Draw a bounding box around every Plasmodium parasite, every leukocyte, and every artifact (stain precipitate or debris).
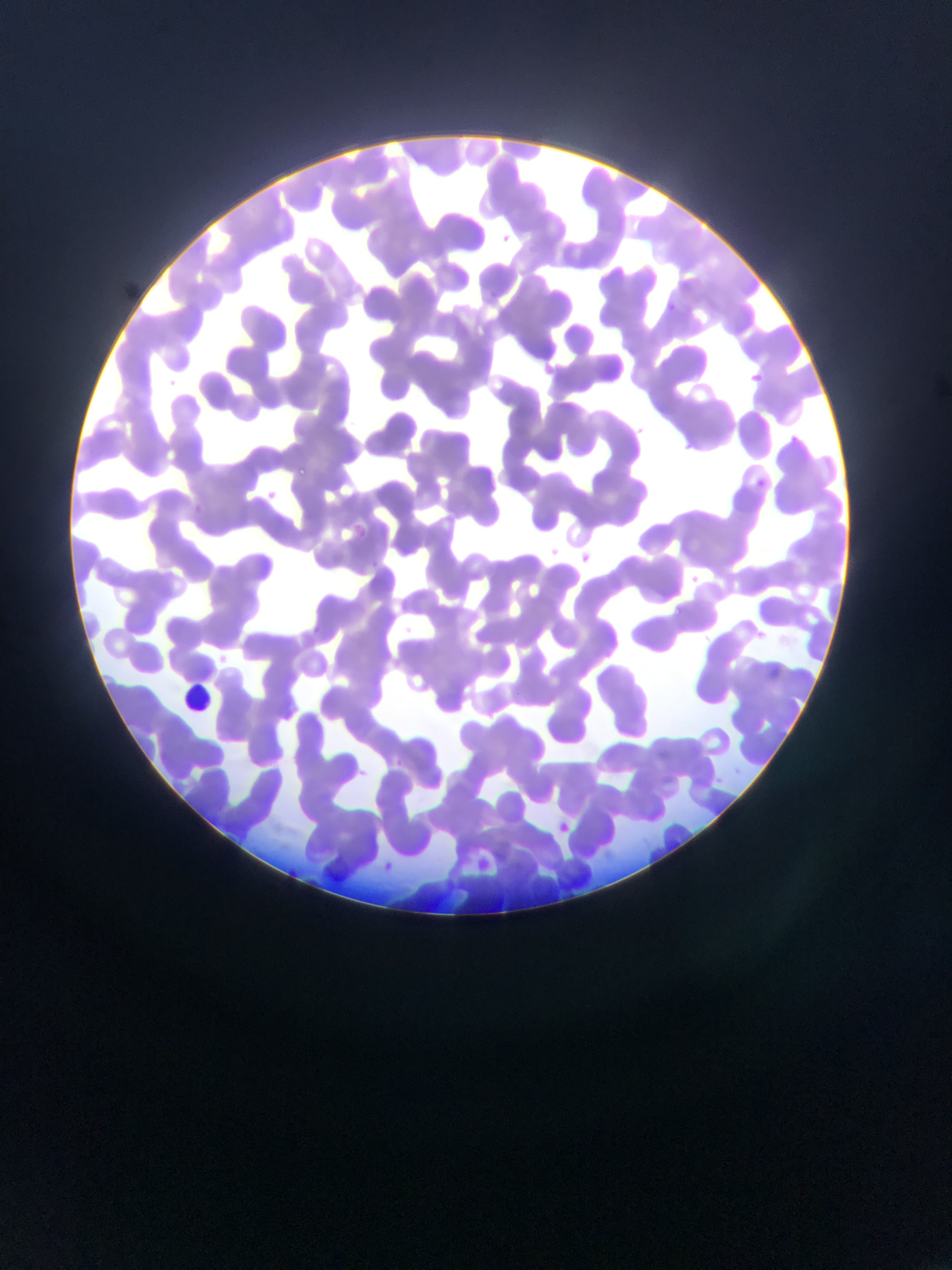

Approximate bounding boxes as (left, top, right, bottom) in pixels.
Plasmodium parasites: (498, 233, 520, 250), (487, 289, 499, 301), (668, 303, 676, 311), (745, 372, 779, 386), (632, 420, 656, 435), (298, 464, 310, 476), (756, 479, 765, 487), (266, 487, 288, 506), (186, 503, 199, 516), (354, 525, 367, 539), (548, 546, 564, 558), (578, 550, 588, 565), (691, 573, 701, 587), (672, 605, 682, 617), (313, 625, 321, 634), (556, 819, 573, 837), (383, 861, 398, 874).
Leukocytes: (180, 682, 215, 718).

country = Ghana
field of view = single
image size = 952×1270 pixels
capture = mobile-phone photograph through a microscope
preparation = thin blood smear